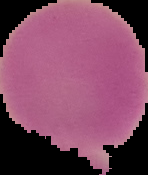
Image is 148×175 pixels. From a thin blood film. Cell region segmented out of the field of view; the surrounding area is masked to black. Result: no Plasmodium parasites seen.